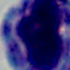
magnification: 1000x
identification: leukocyte
modality: photomicrograph